Classify this cell by malaria status.
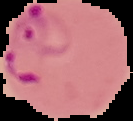

It is parasitized.

image type = segmented cell region on a black background
image size = 133×121 pixels
preparation = thin blood smear